Locate every uninfected red blood cell.
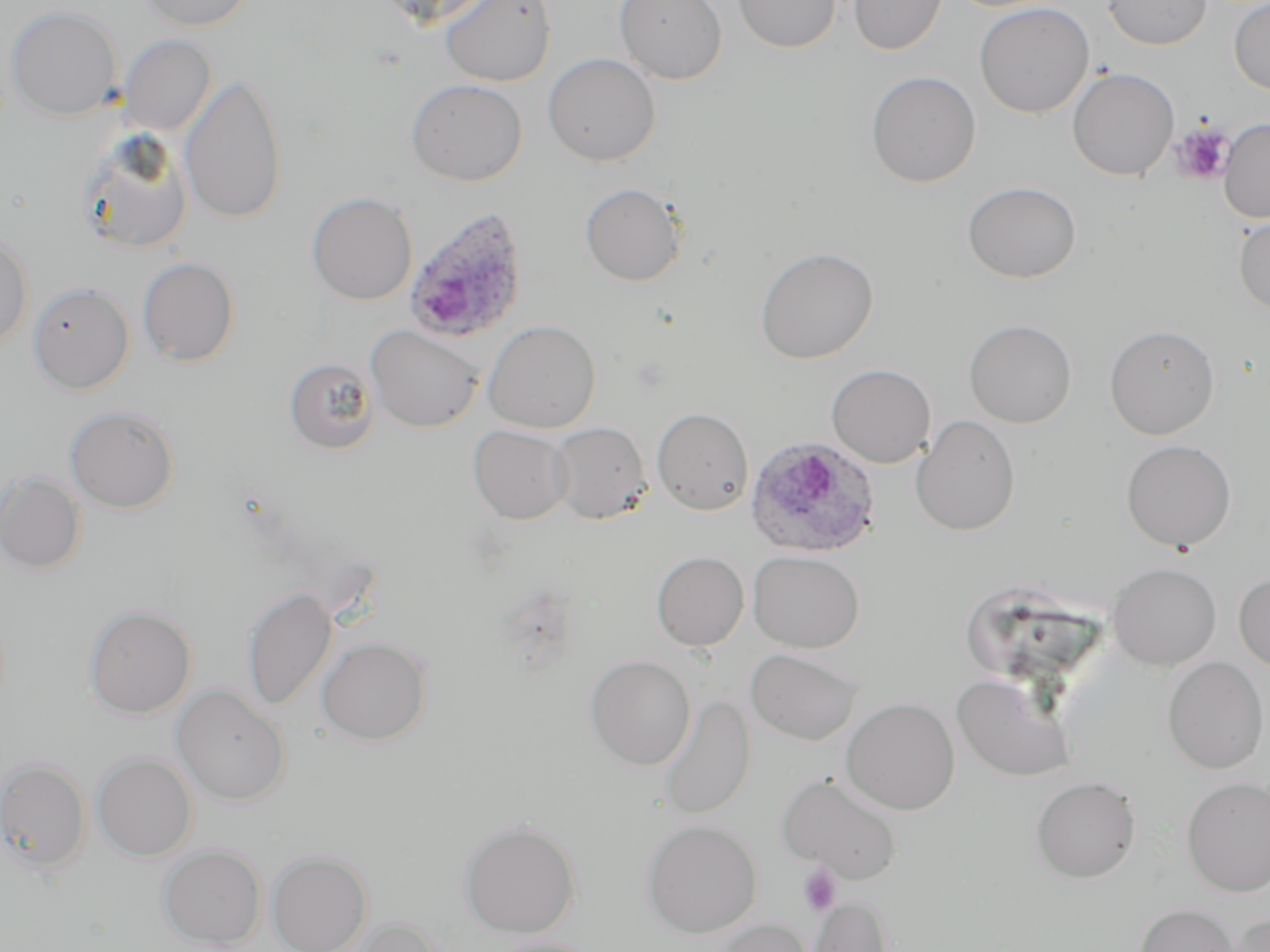
Approximate bounding boxes as (x1,y1)-(x2,y2) corner pairs in pixels.
Uninfected red blood cells: (135,0)-(257,32), (370,0)-(497,29), (439,0)-(556,87), (614,0)-(728,85), (733,0)-(840,54), (847,0)-(947,55), (1103,0)-(1212,50), (1229,0)-(1270,96), (974,2)-(1094,118), (7,6)-(122,121), (119,35)-(217,135), (542,53)-(661,166), (1067,67)-(1179,181), (865,70)-(981,188), (180,73)-(288,225), (405,78)-(527,186), (1218,118)-(1270,224), (77,130)-(194,255), (962,181)-(1082,283), (579,182)-(687,287), (306,192)-(418,305), (1233,216)-(1270,315), (0,231)-(33,349), (754,246)-(879,365), (137,256)-(240,367), (28,282)-(134,395), (963,319)-(1077,428), (482,320)-(601,433), (1104,323)-(1220,439), (365,324)-(484,432), (284,357)-(380,454), (826,364)-(936,468), (64,404)-(181,514), (651,407)-(754,516), (910,415)-(1020,536), (549,422)-(651,525), (467,424)-(573,524), (1120,439)-(1237,552), (1,471)-(87,574), (747,550)-(865,653), (651,551)-(748,652), (1107,562)-(1221,671), (1234,572)-(1270,673), (241,585)-(339,712), (83,605)-(197,719), (316,636)-(432,745), (745,647)-(863,746), (585,655)-(696,770), (1163,656)-(1269,774), (952,673)-(1075,782), (171,684)-(291,806), (657,695)-(756,820), (841,697)-(960,815), (91,752)-(198,861), (0,757)-(90,874), (776,773)-(902,883), (1031,776)-(1142,883), (1182,777)-(1270,897), (458,819)-(581,938), (642,820)-(762,938), (158,844)-(266,948), (266,850)-(373,952), (807,896)-(892,952), (1134,903)-(1240,952), (1229,912)-(1270,952), (340,916)-(445,952), (712,918)-(813,952), (486,937)-(602,952).

{
  "slide_level_diagnosis": "Plasmodium ovale",
  "field_of_view": "single",
  "plasmodium_ovale_infected_red_blood_cell_locations": "approximate bounding boxes as (x1,y1)-(x2,y2) corner pairs in pixels: (402,205)-(530,343), (745,436)-(882,558)",
  "magnification": "1000x",
  "preparation": "thin blood film",
  "image_size": "1270×952 pixels",
  "platelet_locations": "approximate bounding boxes as (x1,y1)-(x2,y2) corner pairs in pixels: (1170,121)-(1235,184), (799,863)-(842,916)",
  "modality": "optical microscopy",
  "stain": "May-Grünwald-Giemsa"
}